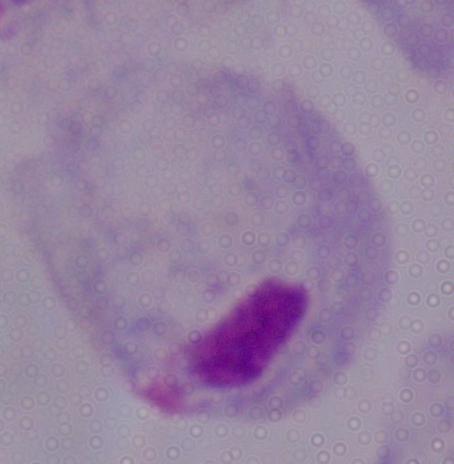 Photomicrograph. 1000x magnification. A trichomonad is shown.